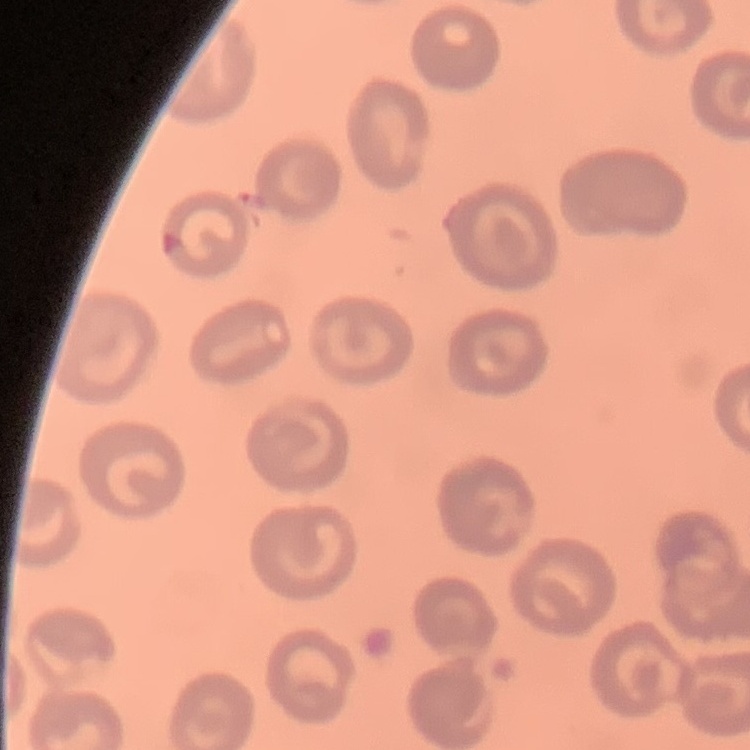
erythrocyte morphology = no rouleaux formation
stain = Field's or Giemsa
image type = square crop of a larger photomicrograph
preparation = thin blood film